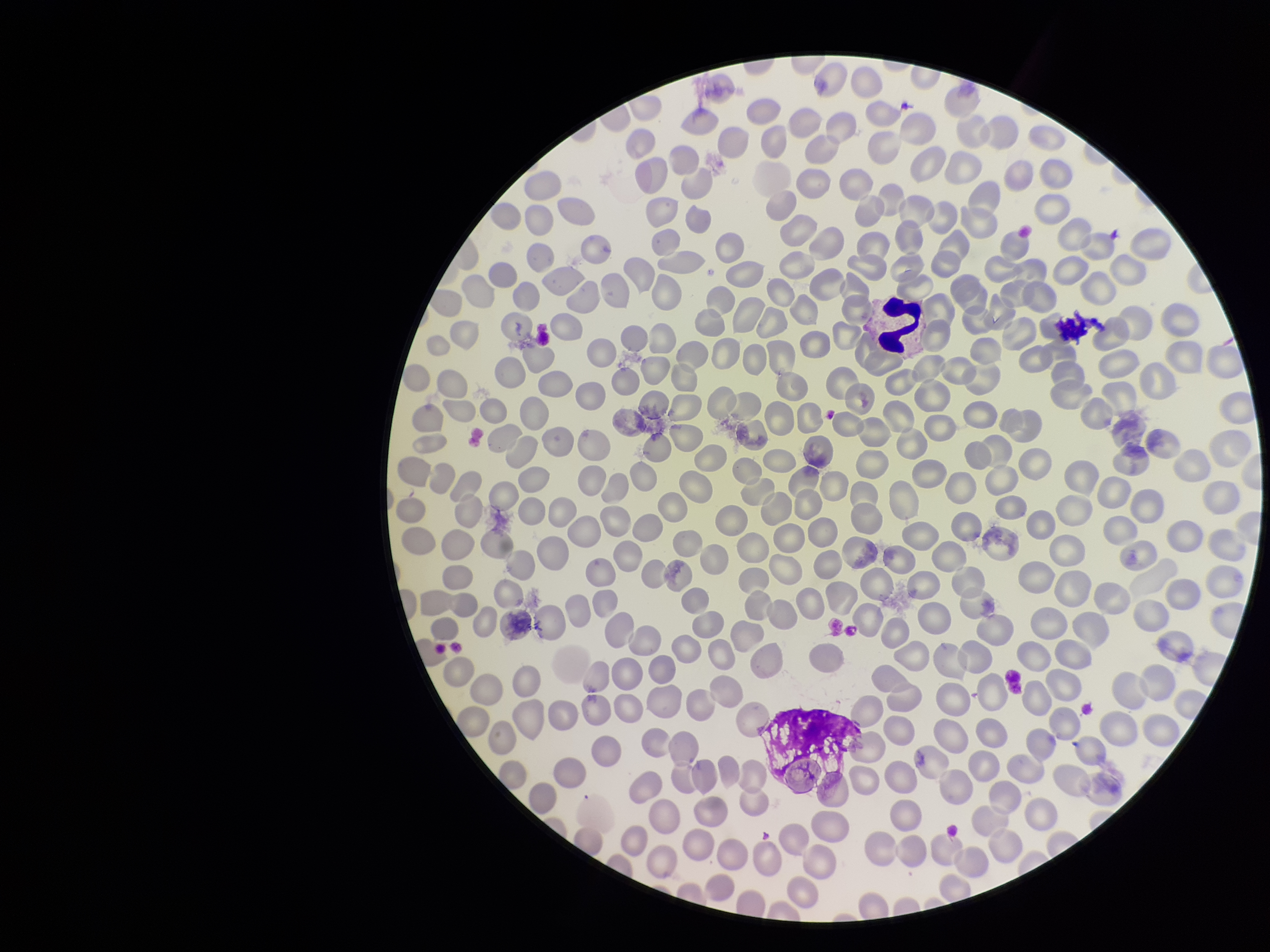

Species reported for this patient: Plasmodium falciparum. Parasitized red blood cell count: 0. Parasitized red blood cells: none detected. Preparation: thin. One field from this slide. Photographed through the microscope eyepiece with a smartphone camera. Red blood cell count: 230. Image is 1270×952 pixels. Patient malaria status: infected. Giemsa stain.